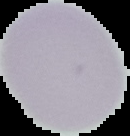

From a thin blood smear. The area outside the segmented cell region is set to black. Malaria status: uninfected. Image is 130×136 pixels.